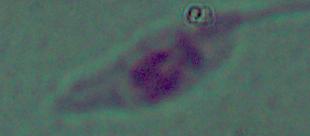
{
  "magnification": "1000x",
  "identification": "Leishmania",
  "modality": "micrograph"
}